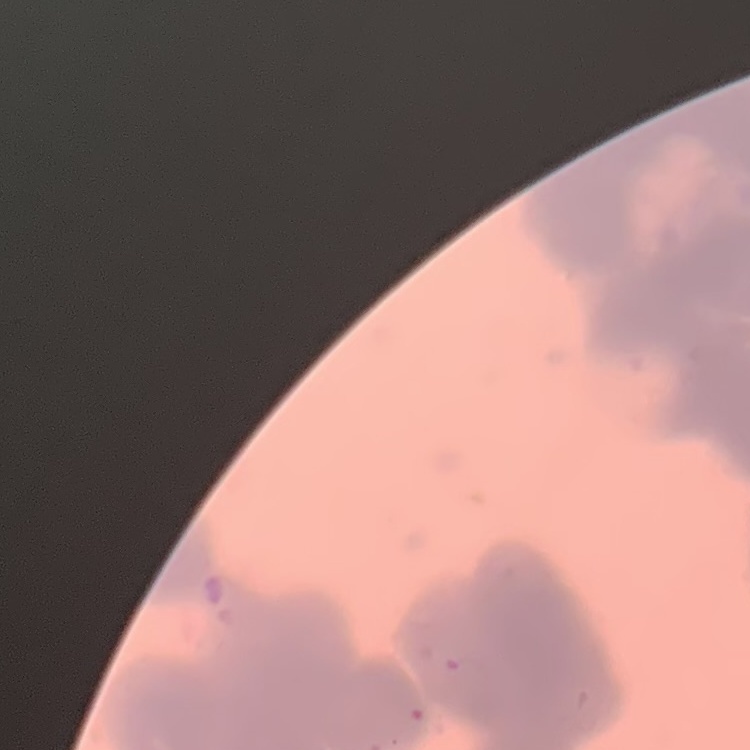
red blood cell morphology = rouleaux formation
stain = Field's or Giemsa
preparation = thin blood smear
image type = square crop of a larger photomicrograph